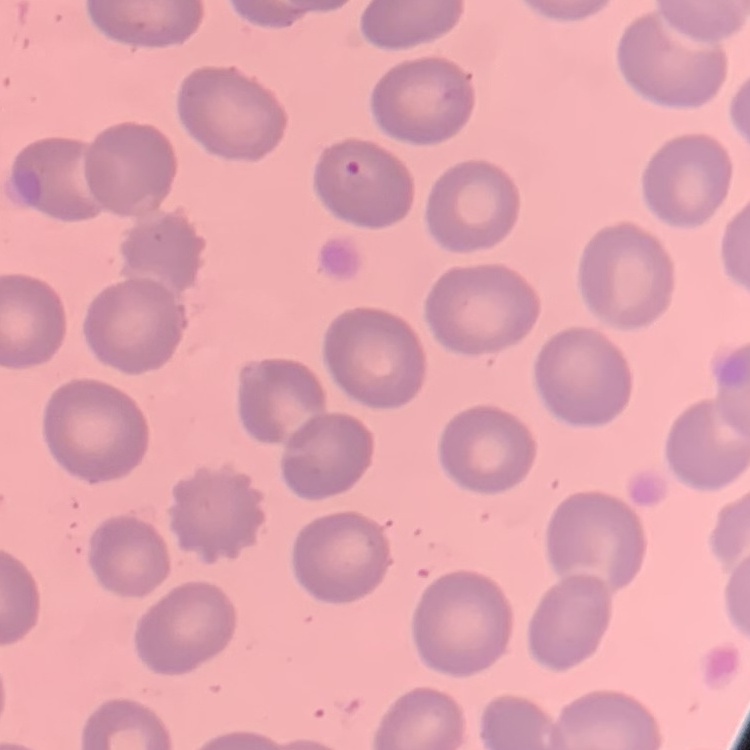
The erythrocytes exhibit no rouleaux formation. One tile cut from a larger photomicrograph. Thin peripheral smear. Stained with either Field's or Giemsa.